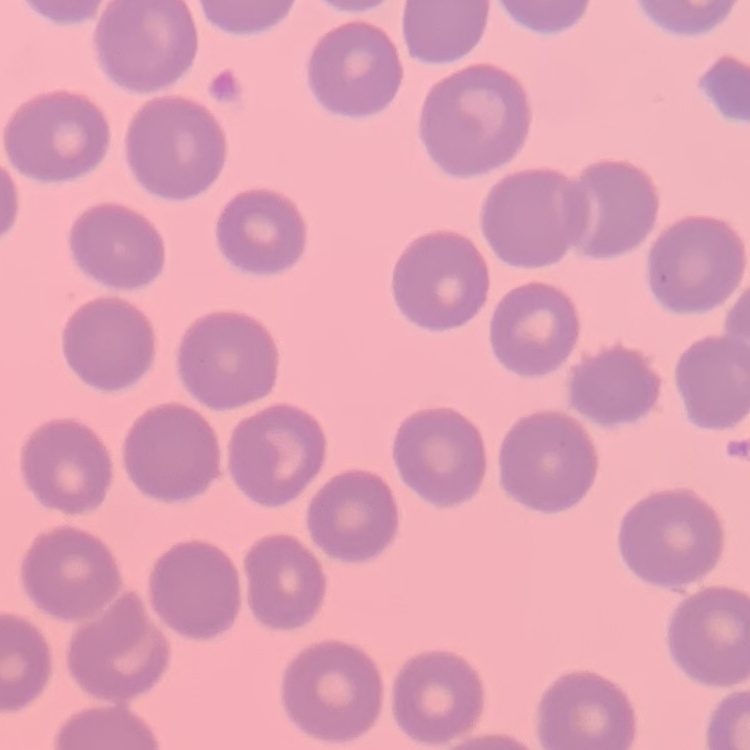

Summary:
  - Red blood cell morphology: no rouleaux formation
  - Stain: Field's or Giemsa
  - Preparation: thin peripheral smear
  - Image type: one tile cut from a larger photomicrograph